Give the extent of all Plasmodium falciparum-infected red blood cells.
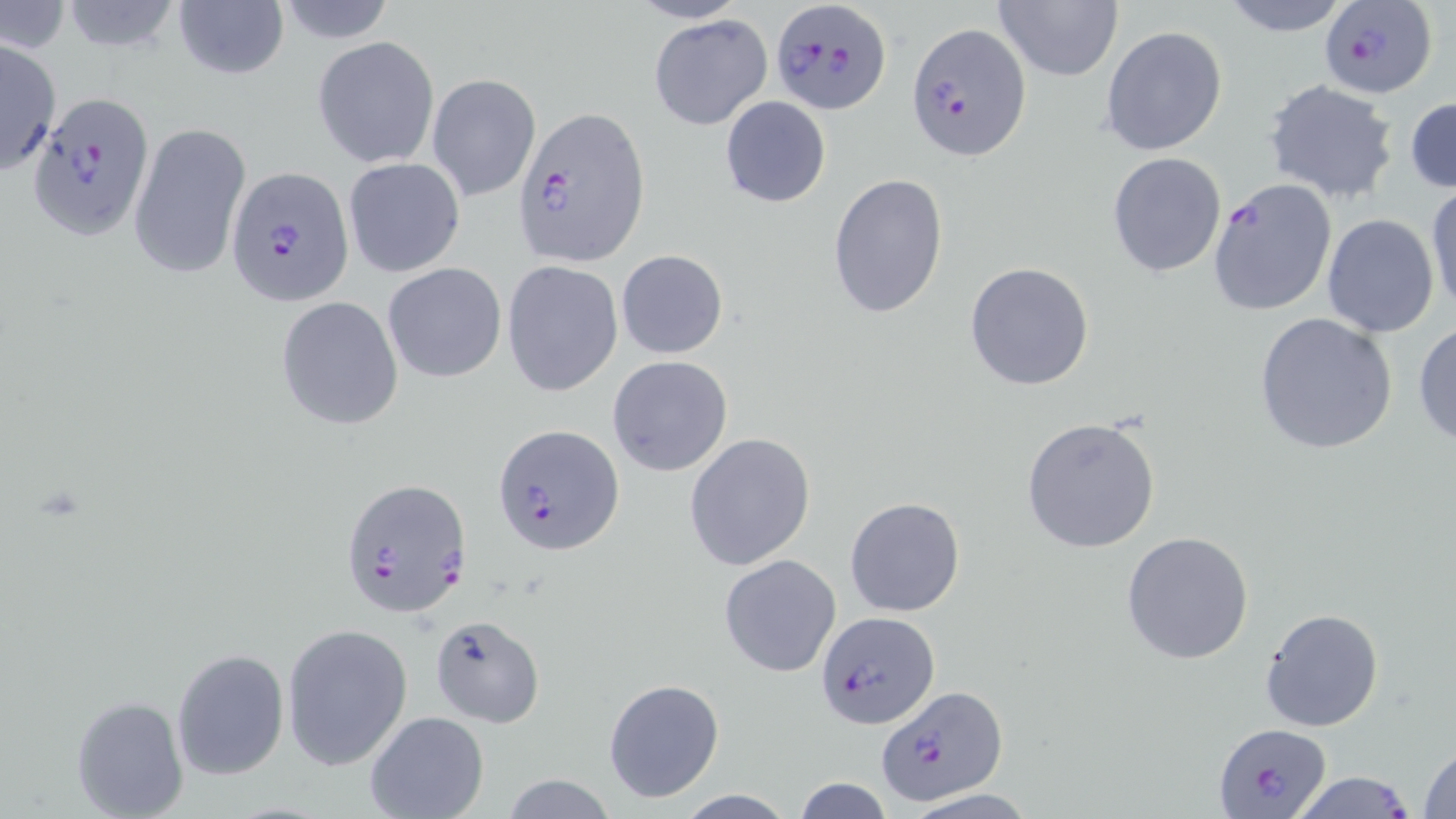

Approximate bounding boxes as named x1/y1/x2/y2 corners in pixels.
Plasmodium falciparum-infected red blood cells: (x1=769, y1=1, x2=892, y2=114), (x1=1318, y1=1, x2=1438, y2=98), (x1=907, y1=22, x2=1029, y2=159), (x1=26, y1=91, x2=153, y2=236), (x1=513, y1=104, x2=649, y2=269), (x1=225, y1=167, x2=354, y2=304), (x1=1207, y1=178, x2=1338, y2=318), (x1=493, y1=423, x2=625, y2=556), (x1=338, y1=476, x2=472, y2=620), (x1=816, y1=611, x2=938, y2=729), (x1=876, y1=686, x2=1008, y2=806), (x1=1212, y1=721, x2=1333, y2=816), (x1=1287, y1=770, x2=1421, y2=819).

slide_level_diagnosis: Plasmodium falciparum
field_of_view: single
magnification: 1000x
image_size: 1456×819 pixels
preparation: thin blood film
uninfected_red_blood_cell_locations: 'approximate bounding boxes as named x1/y1/x2/y2 corners in pixels: (x1=59, y1=0, x2=184, y2=53), (x1=173, y1=0, x2=289, y2=79), (x1=993, y1=0, x2=1123, y2=83), (x1=1216, y1=0, x2=1356, y2=36), (x1=273, y1=1, x2=400, y2=46), (x1=1, y1=3, x2=71, y2=55), (x1=648, y1=13, x2=774, y2=131), (x1=1100, y1=25, x2=1227, y2=157), (x1=312, y1=36, x2=439, y2=168), (x1=0, y1=39, x2=61, y2=174), (x1=427, y1=73, x2=541, y2=202), (x1=1263, y1=80, x2=1400, y2=204), (x1=720, y1=95, x2=831, y2=208), (x1=1406, y1=95, x2=1456, y2=194), (x1=128, y1=120, x2=252, y2=282), (x1=1108, y1=152, x2=1227, y2=278), (x1=342, y1=156, x2=465, y2=277), (x1=827, y1=172, x2=950, y2=320), (x1=1426, y1=183, x2=1456, y2=319), (x1=1321, y1=214, x2=1439, y2=338), (x1=615, y1=249, x2=729, y2=359), (x1=502, y1=261, x2=623, y2=397), (x1=381, y1=262, x2=507, y2=382), (x1=964, y1=262, x2=1095, y2=390), (x1=275, y1=295, x2=404, y2=429), (x1=1253, y1=311, x2=1399, y2=455), (x1=1413, y1=320, x2=1456, y2=446), (x1=607, y1=355, x2=734, y2=477), (x1=1020, y1=417, x2=1162, y2=554), (x1=685, y1=434, x2=817, y2=571), (x1=845, y1=496, x2=966, y2=617), (x1=1122, y1=530, x2=1255, y2=665), (x1=718, y1=554, x2=842, y2=678), (x1=1260, y1=608, x2=1385, y2=732), (x1=430, y1=615, x2=547, y2=731), (x1=281, y1=623, x2=413, y2=771), (x1=171, y1=648, x2=290, y2=781), (x1=603, y1=677, x2=726, y2=805), (x1=72, y1=697, x2=190, y2=819), (x1=365, y1=711, x2=489, y2=819), (x1=1417, y1=745, x2=1456, y2=817), (x1=498, y1=775, x2=621, y2=817), (x1=793, y1=777, x2=893, y2=819), (x1=903, y1=788, x2=1040, y2=818)'
stain: May-Grünwald-Giemsa
modality: optical microscopy